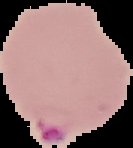

image size = 133×148 pixels
result = Plasmodium parasites identified
image type = cell region segmented out of the field of view; surrounding area masked to black
preparation = thin blood film